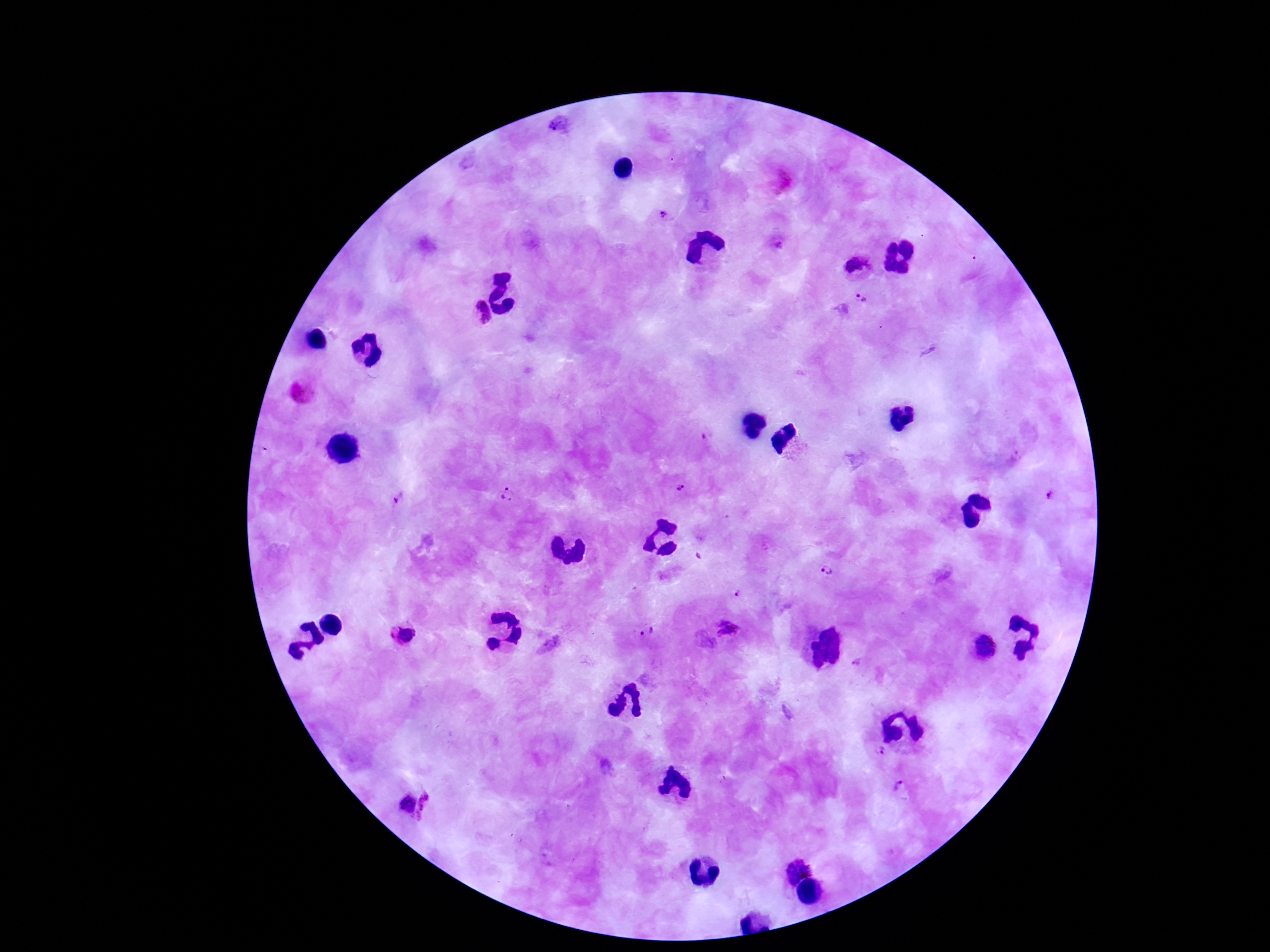

plasmodium_parasite_locations: 'approximate object centers, in pixels from the top-left corner: (x=558, y=123), (x=660, y=216), (x=779, y=245), (x=858, y=268), (x=862, y=298), (x=474, y=316), (x=300, y=391), (x=682, y=488), (x=1052, y=495), (x=509, y=496), (x=398, y=499), (x=829, y=569), (x=736, y=596), (x=648, y=630), (x=727, y=630), (x=400, y=636), (x=982, y=646), (x=855, y=663), (x=878, y=752), (x=899, y=788), (x=398, y=803), (x=432, y=809), (x=796, y=861)'
magnification: 100x
capture: smartphone camera through the microscope eyepiece
image_size: 1270×952 pixels
patient_malaria_status: infected
field_of_view: one from this slide
stain: Giemsa
preparation: thick peripheral-blood smear